Classify this cell by malaria status.
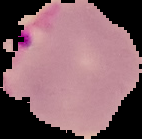
Parasitized.

{
  "image_type": "segmented cell region with the area outside set to black",
  "image_size": "142×139 pixels",
  "preparation": "thin blood film"
}